Name the parasite shown.
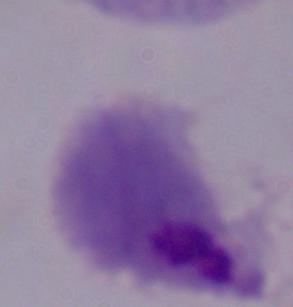
A trichomonad.

modality = photomicrograph
magnification = 1000x